Report the malaria status of this cell.
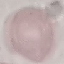

It is uninfected.

Photographed with a smartphone camera at the microscope eyepiece. Thin blood film. Giemsa-stained preparation. Cell patch, automatically extracted from a larger field of view and resized to 64 × 64 pixels.